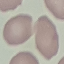
malaria status = uninfected
preparation = thin smear
capture = smartphone camera at the microscope eyepiece
image type = cell patch, automatically extracted from a larger field of view and resized to 64 × 64 pixels
stain = Giemsa